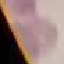

Malaria status: uninfected. Automatically extracted cell patch, resized to 64 × 64 pixels. Giemsa-stained preparation. Photographed with a smartphone camera at the microscope eyepiece. Thin smear of blood.